Give a bounding box for every parasitised red blood cell.
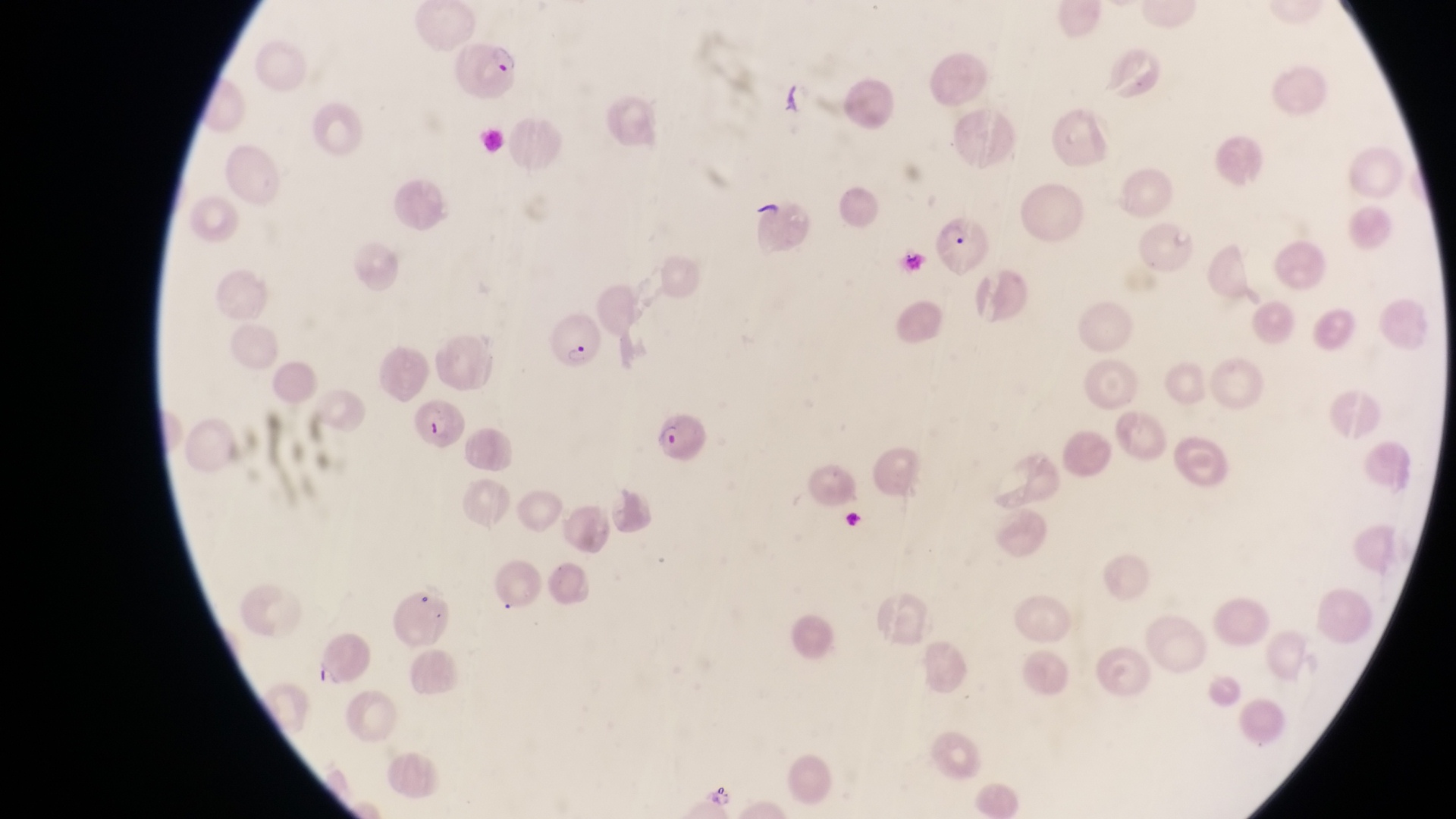
Approximate bounding boxes as {left, top, right, bottom} in pixels.
Parasitised red blood cells: {457, 37, 524, 100}, {933, 217, 993, 277}, {541, 306, 599, 367}, {415, 400, 470, 449}, {642, 407, 703, 463}.

Sample from Uganda. At a magnification of 1000x. Image is 1456×819 pixels. Photographed through the eyepiece of an Olympus CX-23 microscope with a smartphone camera. Single field of view. Thin blood smear.